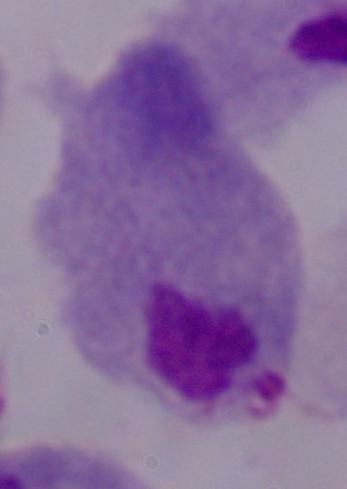
Summary:
  - Identification: trichomonad
  - Modality: photomicrograph
  - Magnification: 1000x